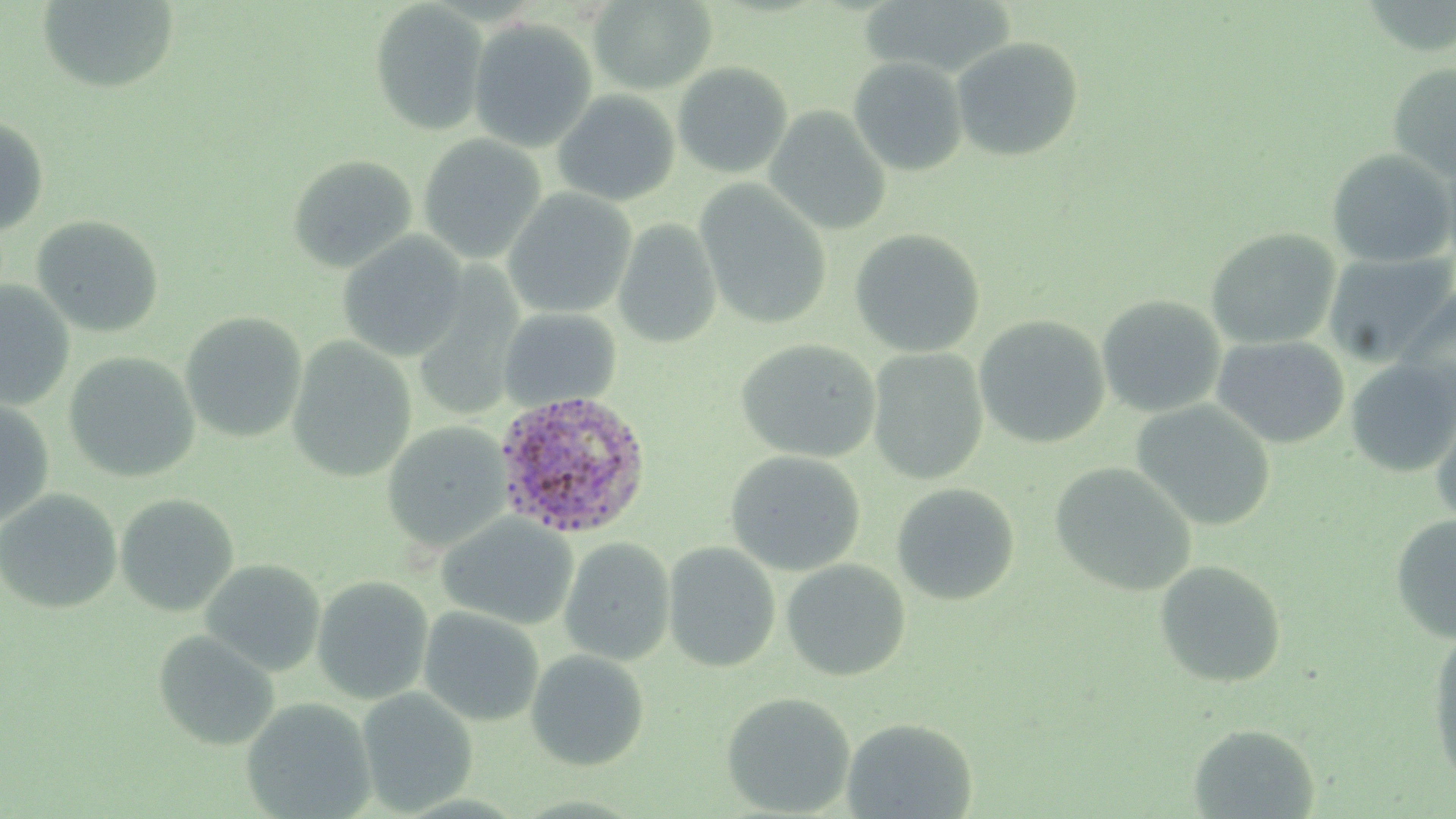

Summary:
  - Coordinate format: approximate bounding boxes as (x1, y1, x2, y2) in pixels
  - Uninfected red blood cell locations: (37, 0, 179, 93), (589, 0, 717, 94), (369, 2, 488, 136), (468, 18, 598, 153), (950, 37, 1084, 162), (848, 57, 967, 176), (672, 62, 794, 180), (1387, 62, 1456, 180), (553, 90, 680, 207), (765, 107, 891, 236), (0, 117, 50, 235), (417, 134, 546, 264), (1326, 149, 1455, 268), (287, 154, 417, 273), (695, 181, 832, 331), (502, 188, 636, 319), (31, 215, 165, 338), (613, 219, 722, 349), (849, 228, 985, 358), (1205, 228, 1341, 350), (336, 232, 468, 361), (1323, 251, 1456, 368), (0, 280, 75, 411), (1394, 286, 1456, 418), (1096, 295, 1226, 418), (498, 307, 621, 411), (180, 312, 307, 443), (973, 315, 1110, 449), (286, 336, 417, 483), (1211, 336, 1350, 449), (736, 339, 881, 463), (867, 348, 989, 485), (63, 351, 200, 483), (1344, 358, 1456, 477), (0, 399, 55, 528), (1130, 400, 1276, 531), (1430, 400, 1456, 530), (382, 422, 511, 555), (725, 450, 865, 576), (1050, 462, 1196, 597), (891, 483, 1020, 606), (0, 489, 122, 614), (114, 494, 239, 616), (437, 513, 578, 630), (1390, 513, 1456, 645), (558, 536, 675, 666), (663, 542, 780, 672), (200, 559, 326, 677), (781, 559, 911, 681), (1153, 560, 1287, 688), (311, 575, 434, 705), (418, 606, 544, 726), (153, 630, 280, 751), (1428, 630, 1456, 783), (526, 650, 650, 771), (356, 687, 478, 815), (721, 691, 856, 817), (240, 697, 377, 818), (842, 717, 977, 818), (1187, 724, 1319, 818)
  - Plasmodium ovale-infected red blood cell locations: (493, 390, 652, 538)
  - Slide-level diagnosis: Plasmodium ovale
  - Stain: May-Grünwald-Giemsa
  - Field of view: one of a larger specimen
  - Preparation: thin blood film
  - Modality: light microscopy
  - Magnification: 1000x
  - Image size: 1456×819 pixels